Classify this cell by malaria status.
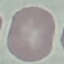

It is uninfected.

stain = Giemsa
capture = smartphone through the microscope eyepiece
image type = cell patch, automatically extracted from a larger field of view and resized to 64 × 64 pixels
preparation = thin smear